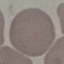
result = negative for malaria parasites
preparation = thin smear
stain = Giemsa
image type = cell patch, automatically extracted from a larger field of view and resized to 64 × 64 pixels
capture = smartphone camera at the microscope eyepiece